Name the parasite shown.
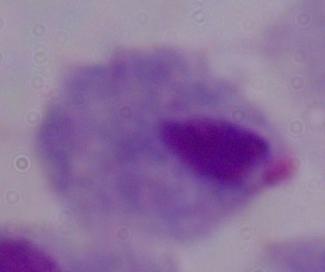
This is a trichomonad.

Summary:
  - Modality: micrograph
  - Magnification: 1000x